Classify this cell by malaria status.
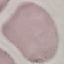

Uninfected.

Summary:
  - Image type: automatically extracted cell patch, resized to 64 × 64 pixels
  - Capture: smartphone through the microscope eyepiece
  - Stain: Giemsa
  - Preparation: thin smear